State which parasite is depicted.
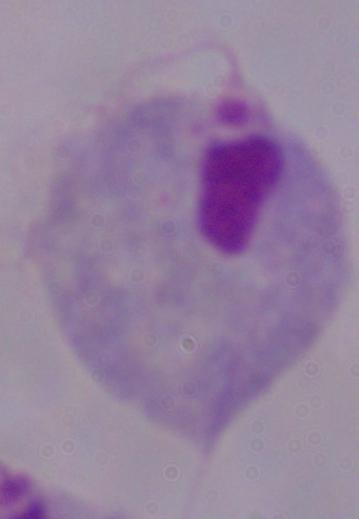

A trichomonad.

Photomicrograph. 1000x magnification.